State which parasite is depicted.
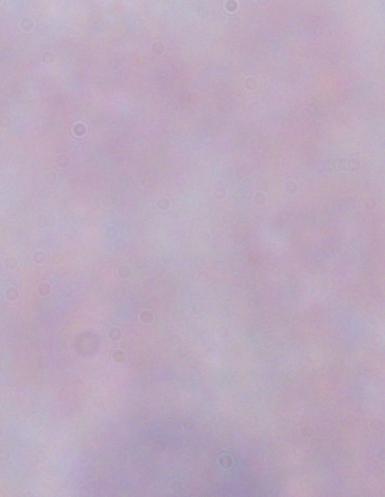

A trypanosome.

Captured at 1000x magnification. Photomicrograph.